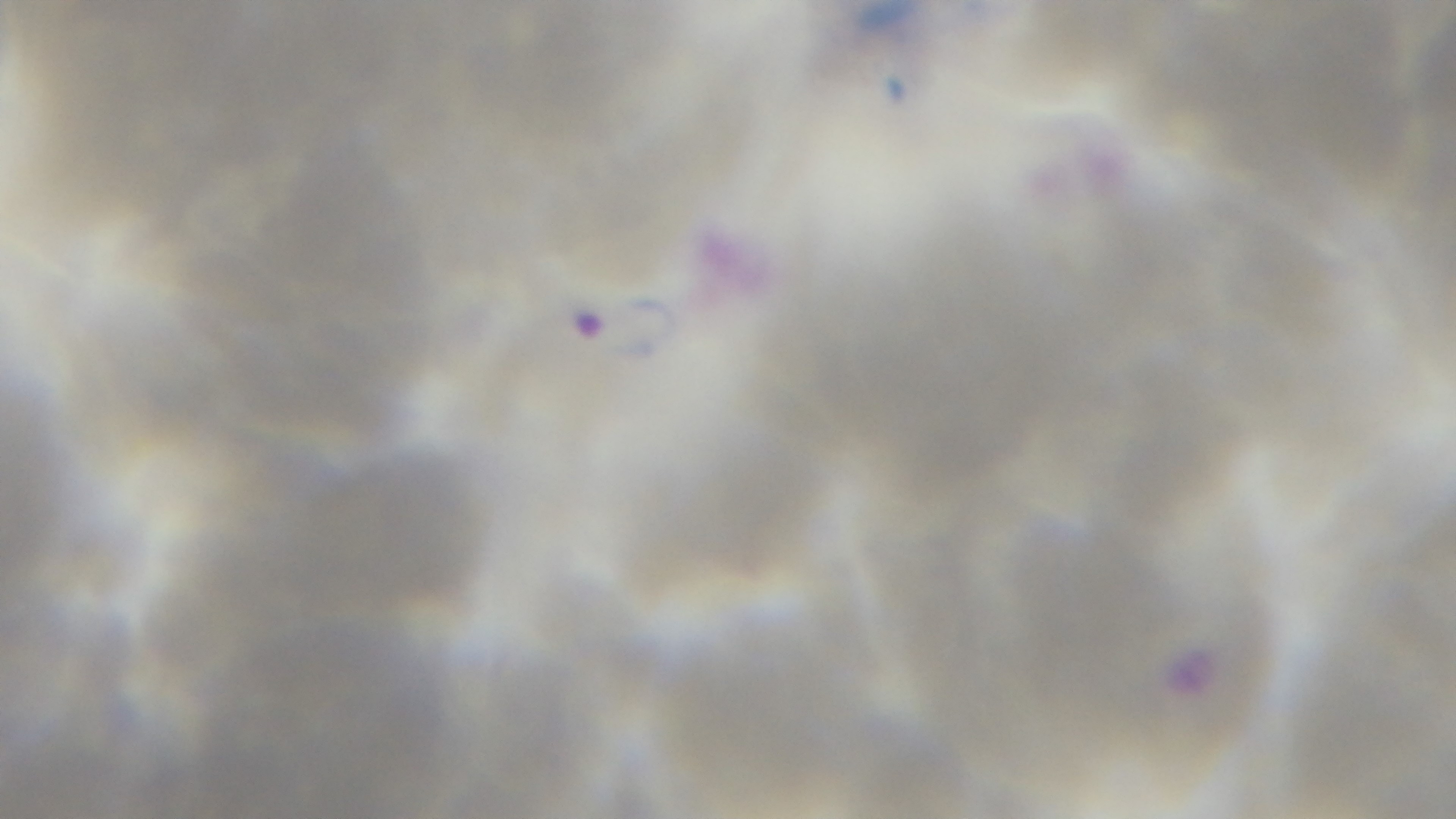

{
  "stain": "Giemsa",
  "objective": "100x oil immersion",
  "preparation": "thin smear",
  "modality": "light microscopy",
  "field_of_view": "single",
  "capture": "mounted 4K digital camera",
  "malaria_status": "positive"
}